Assess this cell for malaria.
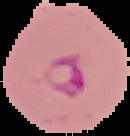
It is parasitized.

From a thin blood film. Image is 130×136 pixels. The area outside the segmented cell region is set to black.